Locate and identify every blood parasite.
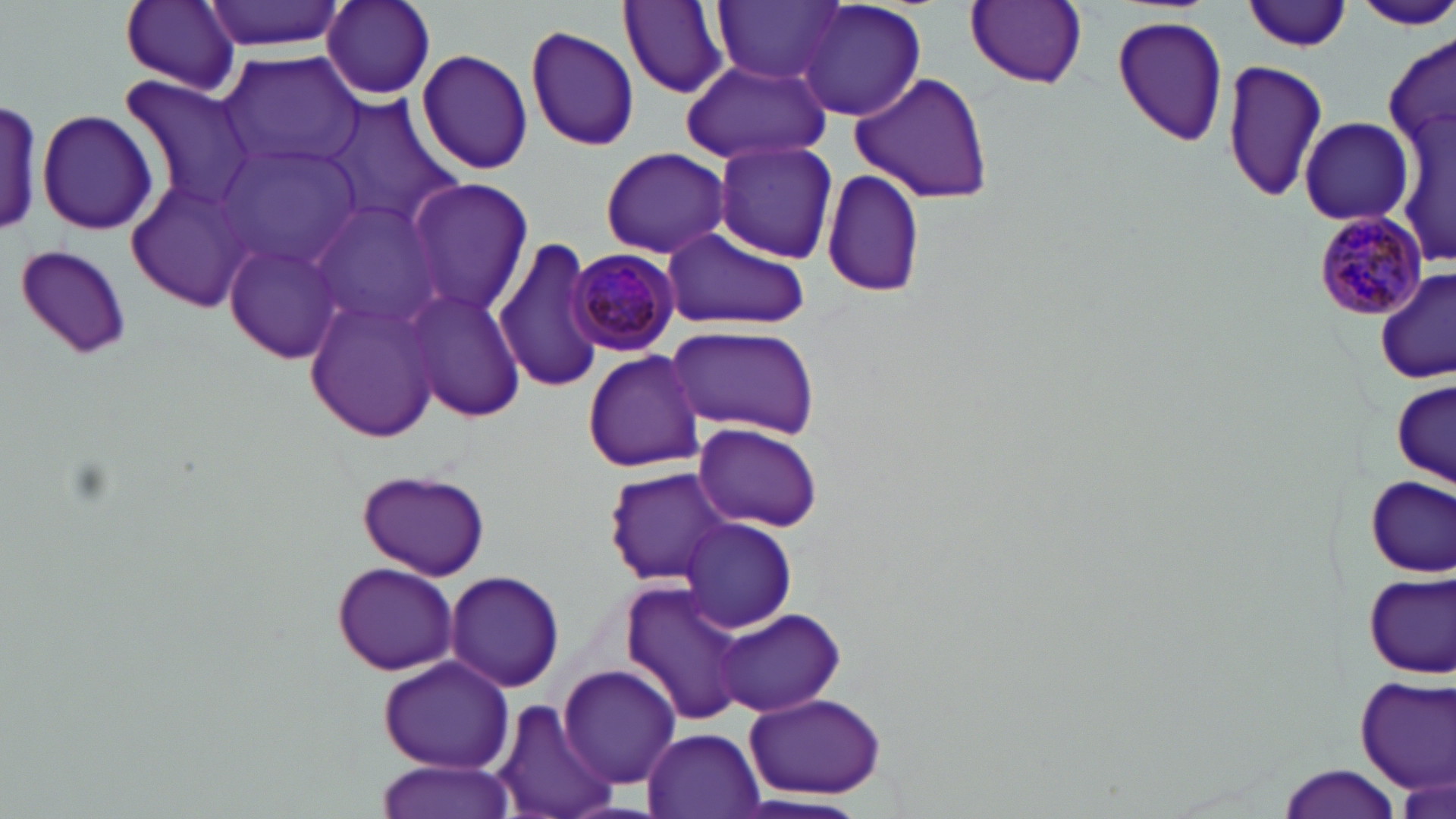
Approximate bounding boxes as named x1/y1/x2/y2 corners in pixels.
Plasmodium malariae-infected red blood cells: (x1=1313, y1=212, x2=1428, y2=323), (x1=568, y1=248, x2=680, y2=355).
No Plasmodium falciparum, Plasmodium ovale, Plasmodium vivax, Babesia divergens, or Trypanosoma brucei observed.

Summary:
  - Uninfected red blood cell locations: (x1=118, y1=0, x2=245, y2=93), (x1=201, y1=0, x2=344, y2=53), (x1=619, y1=0, x2=731, y2=98), (x1=715, y1=0, x2=842, y2=84), (x1=320, y1=1, x2=436, y2=100), (x1=797, y1=1, x2=926, y2=123), (x1=964, y1=1, x2=1088, y2=89), (x1=1243, y1=1, x2=1353, y2=52), (x1=1353, y1=3, x2=1456, y2=30), (x1=1109, y1=13, x2=1229, y2=147), (x1=524, y1=24, x2=641, y2=151), (x1=1385, y1=30, x2=1453, y2=174), (x1=417, y1=49, x2=534, y2=177), (x1=220, y1=51, x2=365, y2=171), (x1=1221, y1=57, x2=1328, y2=202), (x1=679, y1=61, x2=833, y2=164), (x1=1391, y1=68, x2=1453, y2=275), (x1=847, y1=69, x2=995, y2=205), (x1=118, y1=75, x2=260, y2=213), (x1=0, y1=98, x2=50, y2=238), (x1=328, y1=99, x2=461, y2=223), (x1=36, y1=107, x2=157, y2=236), (x1=1297, y1=115, x2=1413, y2=226), (x1=712, y1=137, x2=838, y2=263), (x1=218, y1=141, x2=364, y2=270), (x1=598, y1=146, x2=732, y2=260), (x1=819, y1=171, x2=929, y2=299), (x1=404, y1=178, x2=534, y2=317), (x1=129, y1=181, x2=257, y2=309), (x1=308, y1=199, x2=449, y2=335), (x1=661, y1=226, x2=811, y2=331), (x1=495, y1=234, x2=607, y2=394), (x1=225, y1=239, x2=345, y2=365), (x1=13, y1=242, x2=135, y2=362), (x1=1375, y1=272, x2=1455, y2=383), (x1=406, y1=288, x2=524, y2=422), (x1=304, y1=295, x2=445, y2=443), (x1=663, y1=321, x2=821, y2=440), (x1=582, y1=348, x2=704, y2=471), (x1=1390, y1=376, x2=1454, y2=490), (x1=692, y1=421, x2=823, y2=532), (x1=602, y1=466, x2=736, y2=585), (x1=355, y1=467, x2=492, y2=580), (x1=1362, y1=475, x2=1452, y2=580), (x1=680, y1=518, x2=798, y2=634), (x1=332, y1=560, x2=458, y2=676), (x1=444, y1=568, x2=565, y2=694), (x1=1362, y1=573, x2=1454, y2=678), (x1=619, y1=583, x2=745, y2=726), (x1=717, y1=610, x2=847, y2=717), (x1=376, y1=653, x2=516, y2=774), (x1=557, y1=664, x2=682, y2=790), (x1=1354, y1=675, x2=1456, y2=795), (x1=742, y1=691, x2=887, y2=800), (x1=491, y1=699, x2=619, y2=819), (x1=643, y1=728, x2=766, y2=818), (x1=372, y1=758, x2=515, y2=819), (x1=1275, y1=762, x2=1403, y2=819), (x1=742, y1=794, x2=869, y2=818)
  - Slide-level diagnosis: Plasmodium malariae
  - Field of view: single
  - Stain: May-Grünwald-Giemsa
  - Image size: 1456×819 pixels
  - Modality: optical microscopy
  - Preparation: thin blood film
  - Magnification: 1000x